Assess this cell for malaria.
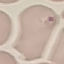
Uninfected.

{
  "preparation": "thin blood film",
  "capture": "smartphone through the microscope eyepiece",
  "stain": "Giemsa",
  "image_type": "automatically extracted cell patch, resized to 64 × 64 pixels"
}